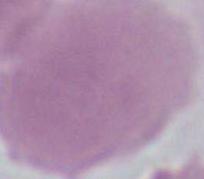
magnification = 1000x
identification = erythrocyte
modality = photomicrograph